Identify the cell.
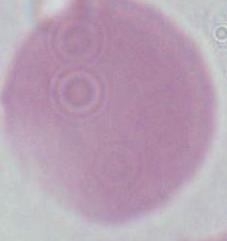
This is an erythrocyte.

{
  "modality": "micrograph",
  "magnification": "1000x"
}